Give the position of every Plasmodium parasite visible.
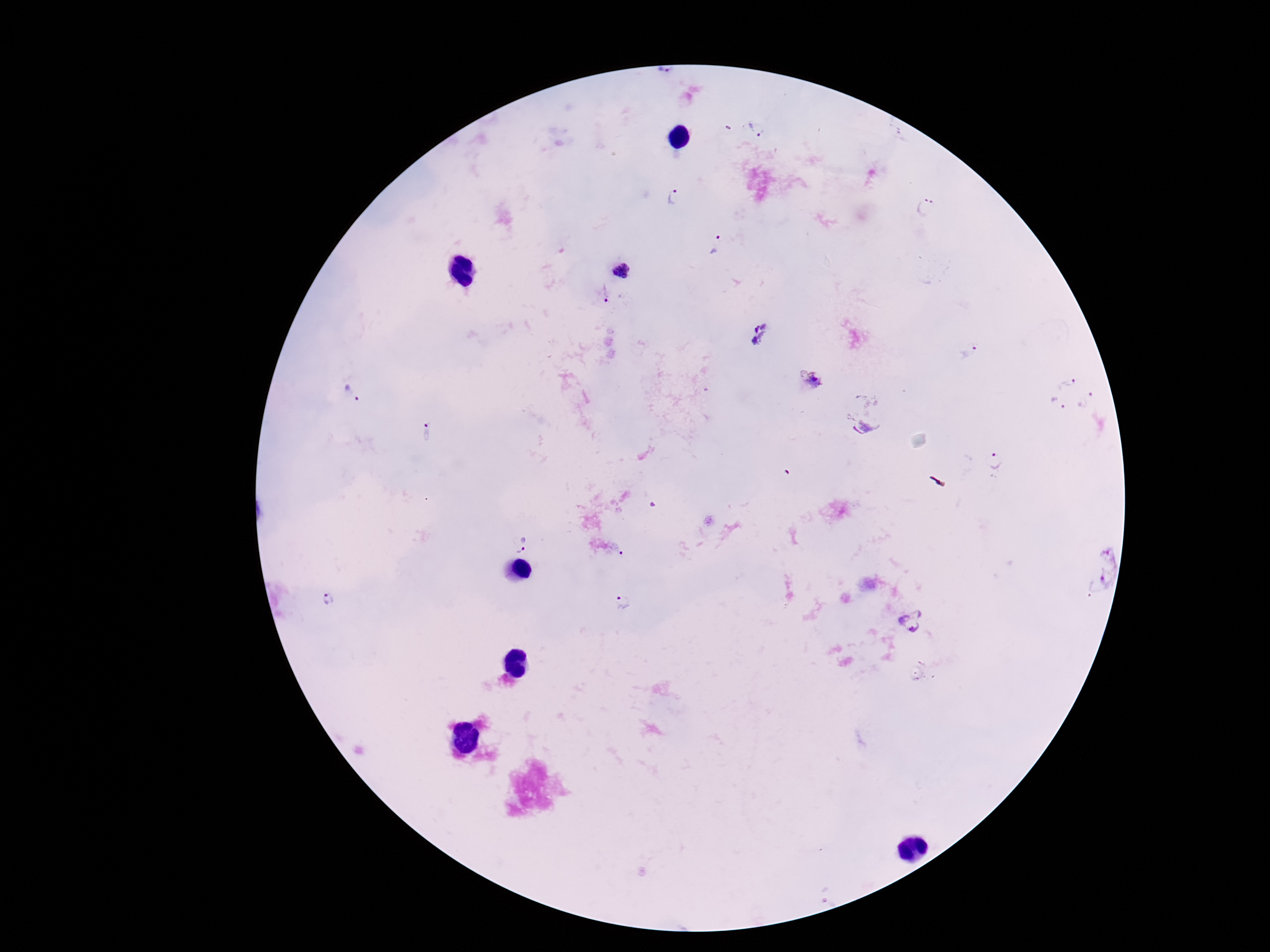
Approximate centers as {x, y} in pixels.
Plasmodium parasites: {755, 130}, {674, 196}, {925, 210}, {716, 244}, {622, 270}, {604, 293}, {759, 334}, {970, 353}, {814, 380}, {1067, 383}, {352, 394}, {1088, 401}, {1058, 405}, {866, 428}, {427, 431}, {994, 462}, {522, 544}, {1095, 564}, {329, 601}, {626, 603}, {912, 621}.

image size = 1270×952 pixels
stain = Giemsa
preparation = thick blood film
patient malaria status = positive
magnification = 100x
capture = smartphone camera through the microscope eyepiece
field of view = one from this slide